Point out Plasmodium parasites and leukocytes.
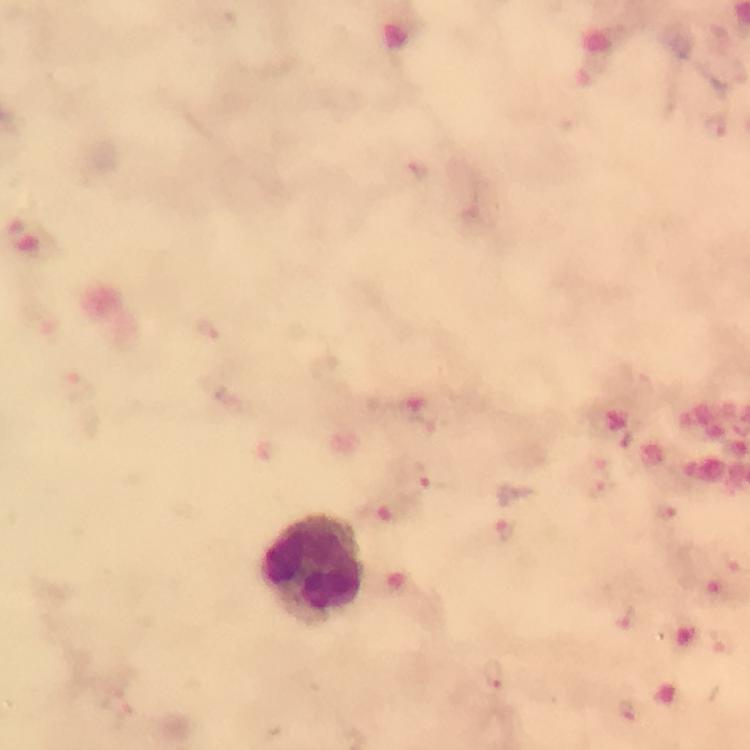
Approximate centers as {x, y} in pixels.
Plasmodium parasites: {712, 130}, {601, 462}, {425, 480}, {603, 490}, {664, 513}, {507, 529}, {627, 619}, {720, 640}, {492, 677}, {631, 711}.
Leukocytes: {314, 569}.

Giemsa stain. Image is 750×750 pixels. Thick blood film. A crop from one field of view. At 100x magnification. From a malaria diagnostic workup. Immersion oil applied. Photographed with a smartphone mounted on the microscope.